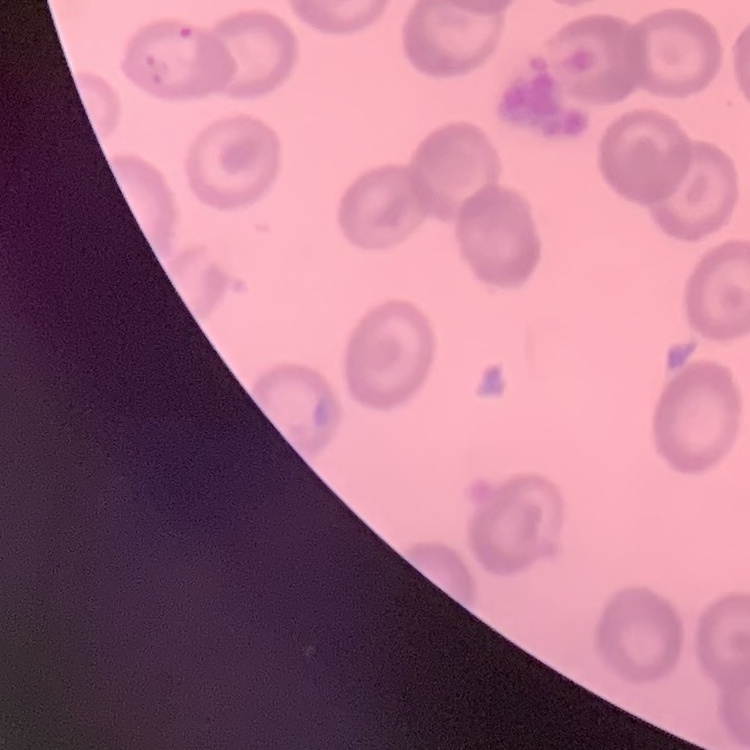 The erythrocytes show no rouleaux formation. Square crop of a larger photomicrograph. Field's or Giemsa stain. Thin blood smear.